Evaluate for malaria.
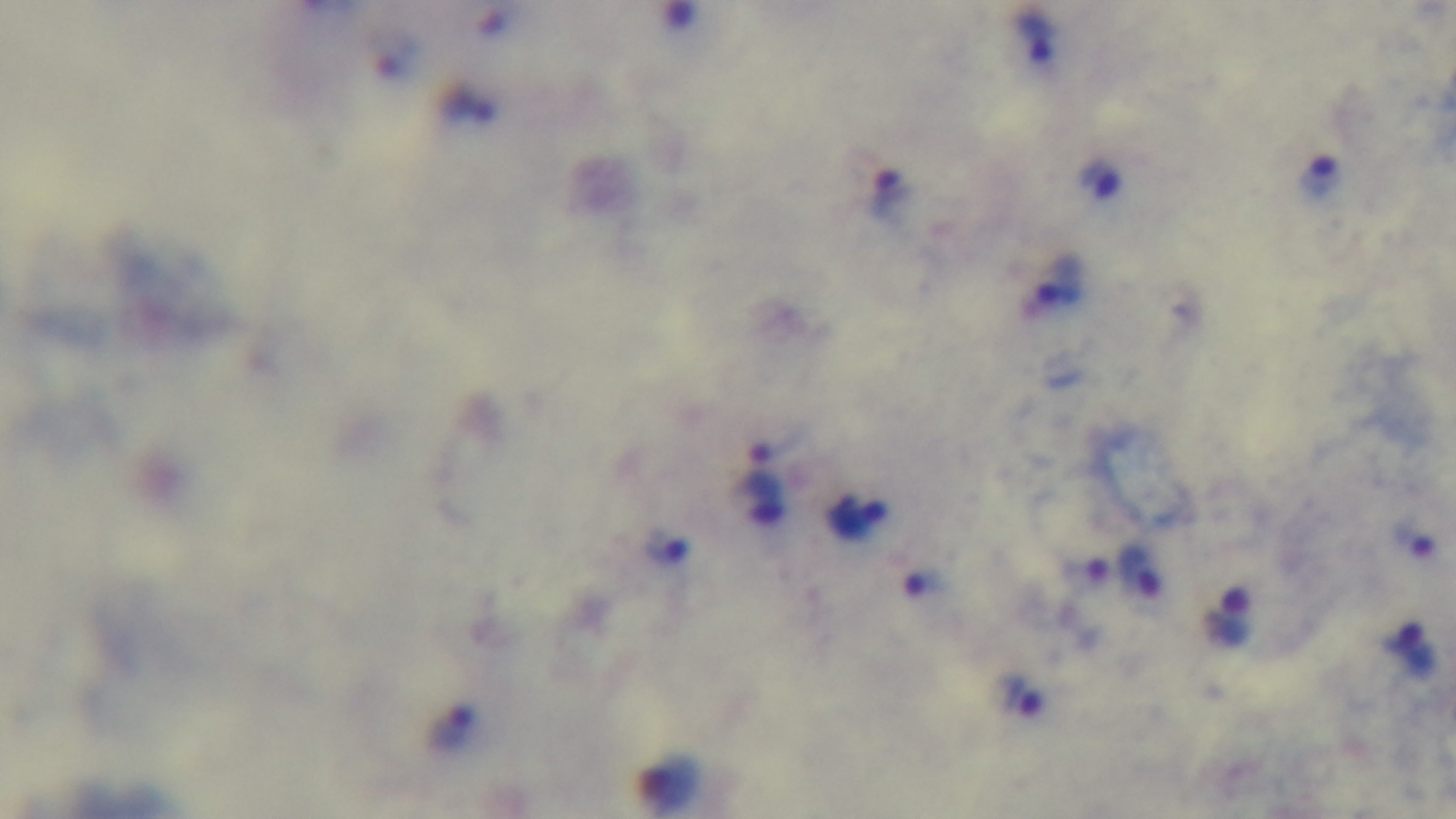
It is infected.

modality = light microscopy
preparation = thick
stain = Giemsa
capture = mounted 4K digital camera
objective = 100x oil immersion
field of view = one from the slide